Name the cell type shown.
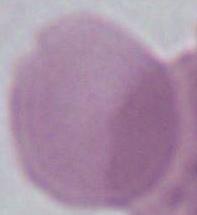

An erythrocyte.

Summary:
  - Magnification: 1000x
  - Modality: micrograph